Report the malaria status.
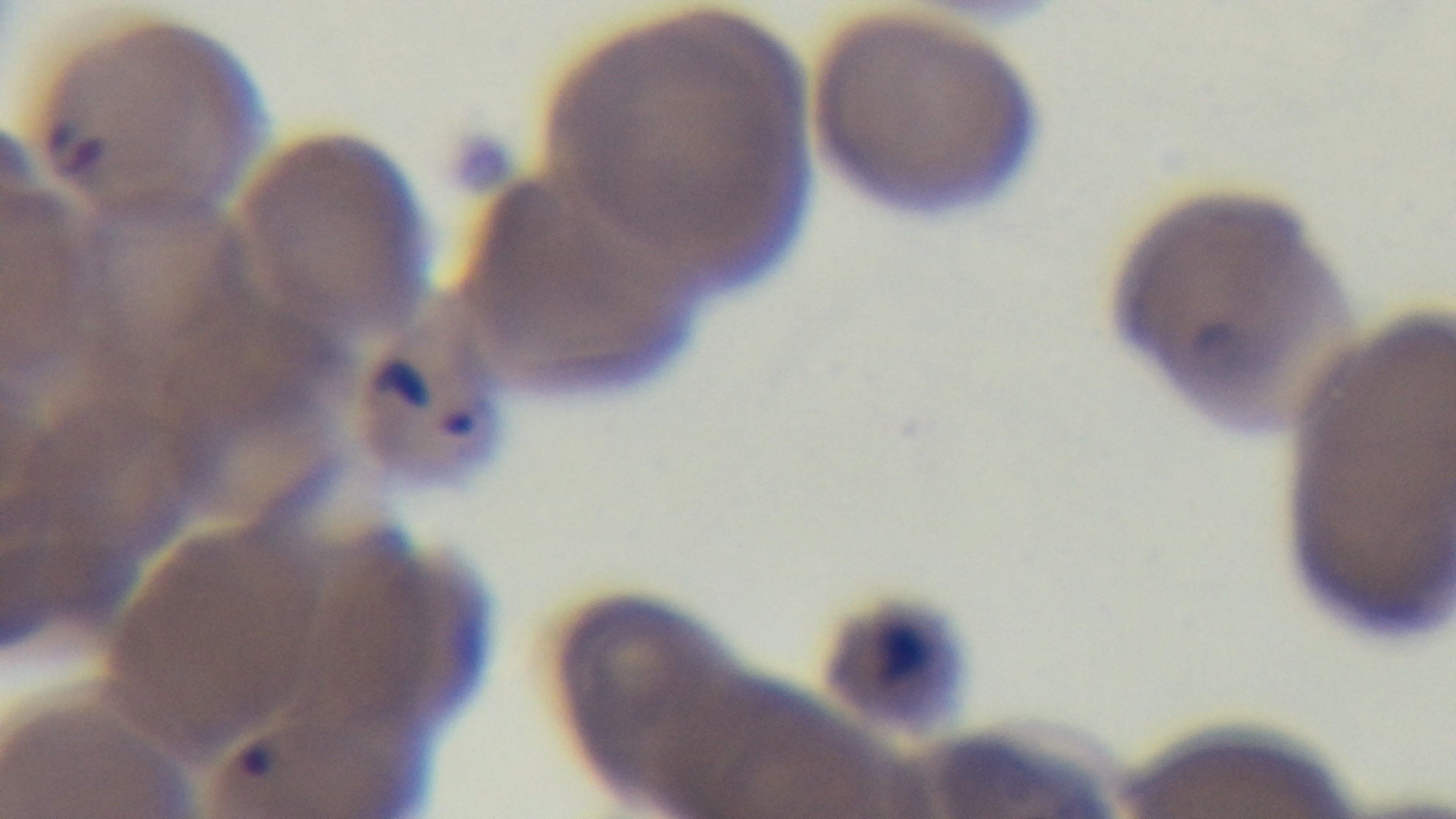

It is infected.

Preparation: thin smear. Photomicrograph. 100x oil-immersion objective. Captured with a mounted 4K digital camera. Single field of view. Giemsa stain.